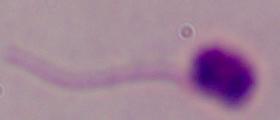

Summary:
  - Identification: Leishmania
  - Modality: micrograph
  - Magnification: 1000x